Give the position of every leukocyte visible.
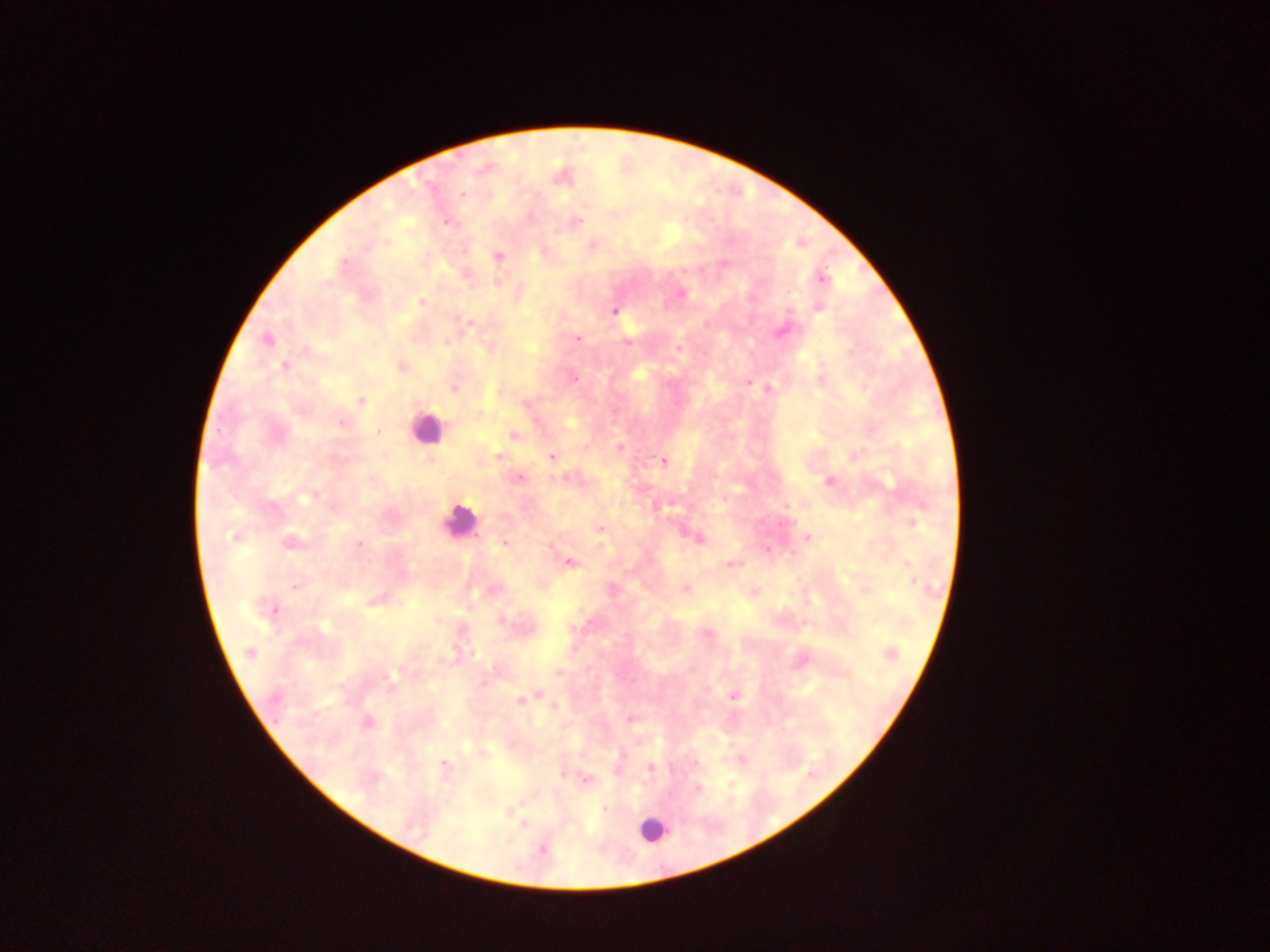

Approximate centers as x y in pixels.
Leukocytes: 426 428; 460 521; 652 829.

capture = mobile-phone photograph through a microscope
image size = 1270×952 pixels
country = Ghana
Plasmodium parasite locations = approximate centers as x y in pixels: 461 194; 577 221; 446 222; 498 256; 822 278; 681 294; 422 302; 818 308; 614 310; 469 324; 782 331; 267 339; 578 339; 446 342; 627 342; 679 349; 284 367; 401 367; 574 379; 749 383; 454 389; 767 389; 361 400; 525 405; 479 413; 341 423; 379 432; 514 435; 620 447; 498 457; 551 457; 664 461; 520 477; 828 482; 309 497; 912 523; 600 529; 234 537; 700 538; 808 538; 291 543; 504 543; 358 544; 767 548; 569 563; 730 564; 908 564; 914 581; 295 587; 685 588; 612 589; 372 601; 273 610; 250 653; 890 653; 558 673; 390 676; 536 695; 733 696; 274 698; 520 700; 554 707; 630 719; 368 722; 695 762; 444 763; 651 767; 562 776; 587 779; 697 789; 604 809; 543 849
field of view = single
preparation = thick blood film